Give a bounding box for every leukocyte visible.
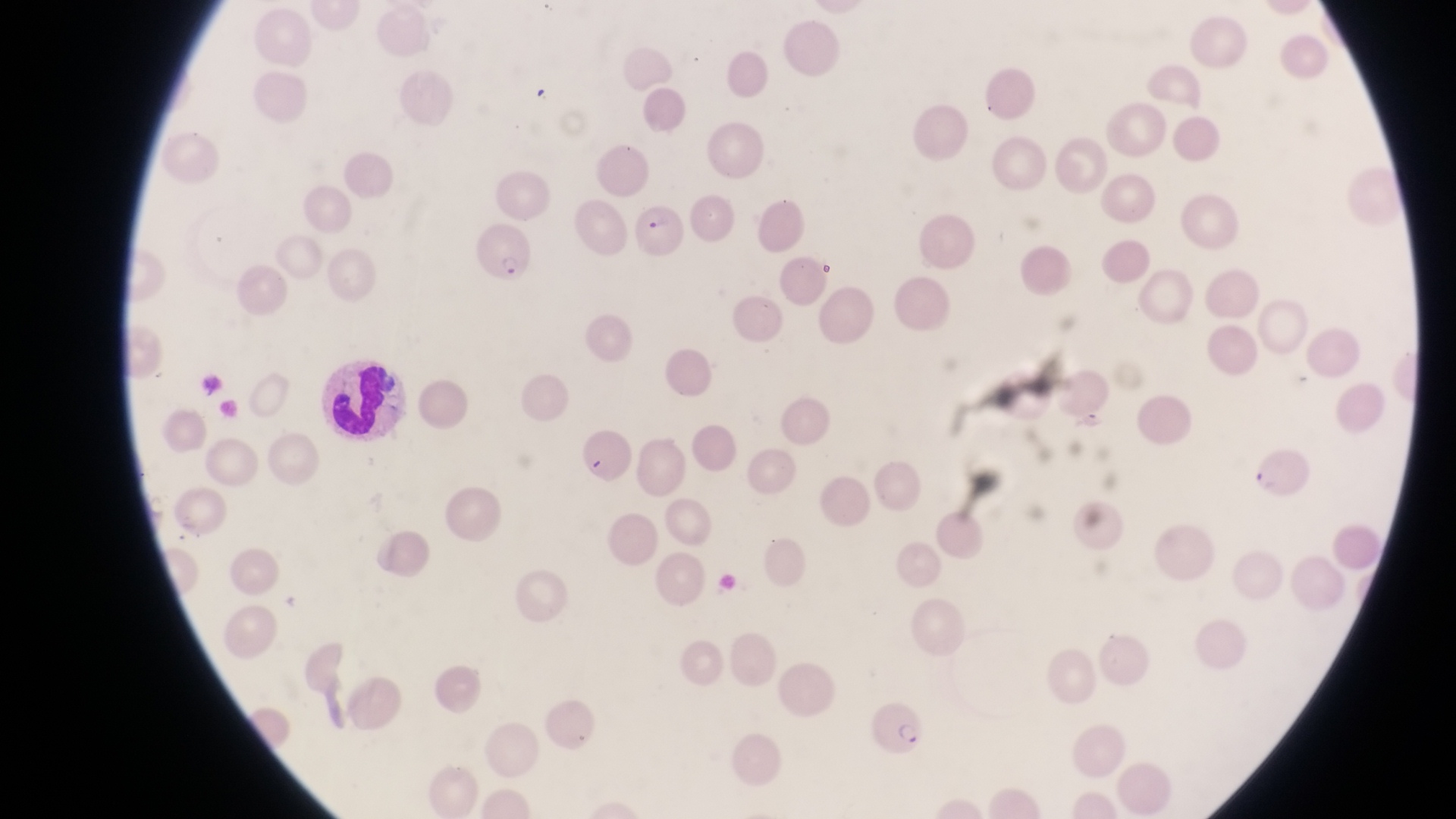

Approximate bounding boxes as left top right bottom in pixels.
Leukocytes: 318 354 404 441.

preparation = thin blood film
image size = 1456×819 pixels
field of view = single
magnification = 1000x
country = Uganda
capture = smartphone photograph through the eyepiece of an Olympus CX-23 microscope
parasitised red blood cell locations = approximate bounding boxes as left top right bottom in pixels: 634 206 692 267; 469 227 533 286; 1250 441 1310 499; 867 698 930 757